Report the malaria status of this cell.
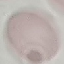
It is uninfected.

preparation: thin blood film
image_type: cell patch, automatically extracted from a larger field of view and resized to 64 × 64 pixels
stain: Giemsa
capture: smartphone through the microscope eyepiece